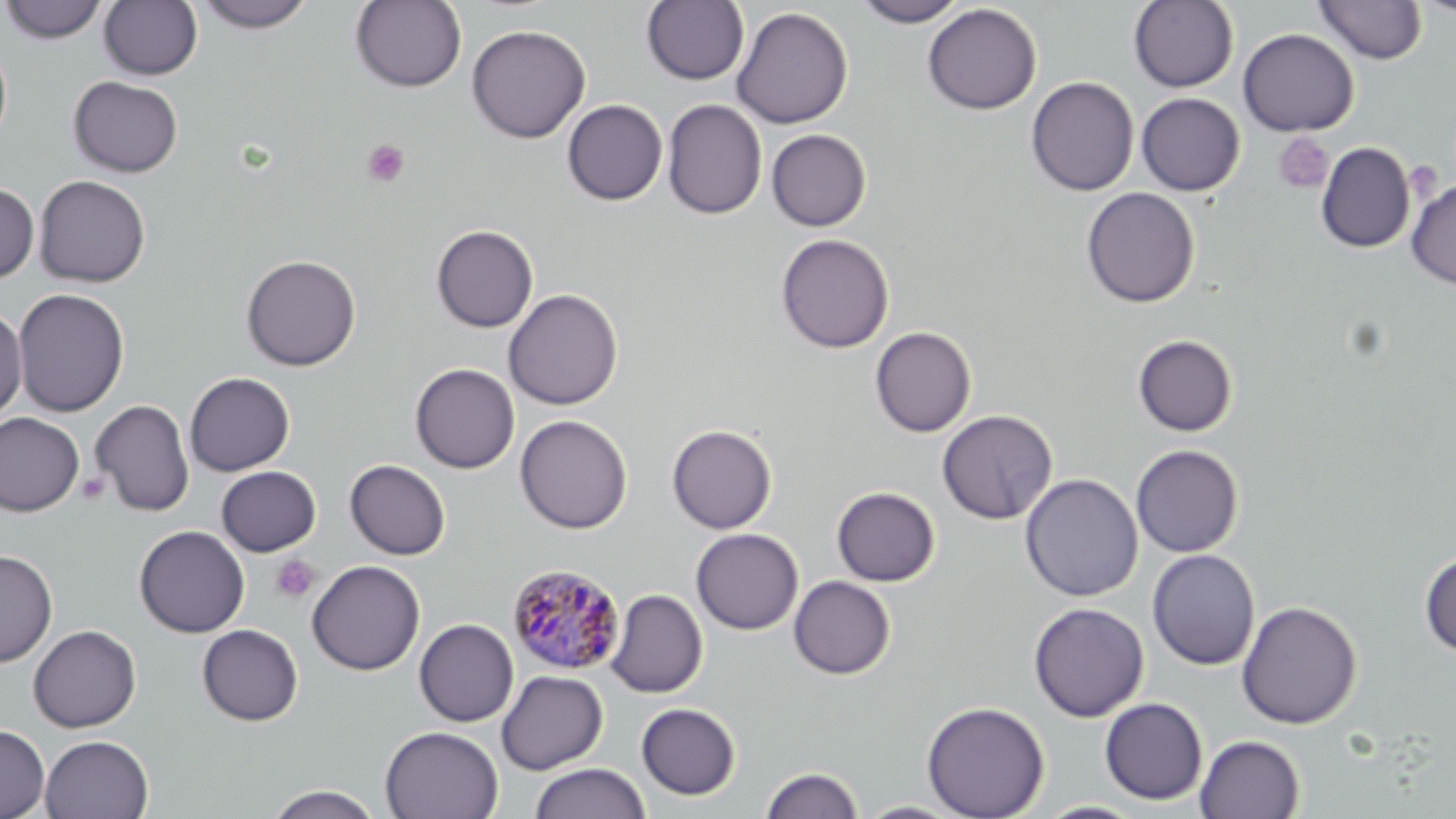

Approximate bounding boxes as named x1/y1/x2/y2 corners in pixels. Uninfected red blood cell locations: (x1=1, y1=0, x2=108, y2=44), (x1=193, y1=0, x2=316, y2=32), (x1=855, y1=0, x2=967, y2=27), (x1=1128, y1=0, x2=1239, y2=93), (x1=1314, y1=0, x2=1427, y2=64), (x1=1412, y1=0, x2=1456, y2=19), (x1=99, y1=1, x2=202, y2=80), (x1=350, y1=1, x2=467, y2=92), (x1=641, y1=1, x2=749, y2=86), (x1=922, y1=4, x2=1042, y2=115), (x1=731, y1=7, x2=854, y2=129), (x1=466, y1=24, x2=591, y2=143), (x1=1237, y1=28, x2=1359, y2=137), (x1=0, y1=40, x2=12, y2=148), (x1=68, y1=76, x2=183, y2=177), (x1=1026, y1=76, x2=1139, y2=196), (x1=1136, y1=92, x2=1245, y2=196), (x1=562, y1=99, x2=668, y2=205), (x1=662, y1=99, x2=767, y2=220), (x1=766, y1=129, x2=871, y2=231), (x1=1316, y1=142, x2=1415, y2=253), (x1=33, y1=175, x2=151, y2=288), (x1=1406, y1=179, x2=1456, y2=289), (x1=0, y1=182, x2=39, y2=284), (x1=1081, y1=187, x2=1200, y2=308), (x1=431, y1=225, x2=538, y2=332), (x1=775, y1=233, x2=894, y2=354), (x1=241, y1=254, x2=361, y2=371), (x1=12, y1=288, x2=129, y2=417), (x1=503, y1=288, x2=623, y2=410), (x1=0, y1=306, x2=28, y2=420), (x1=870, y1=326, x2=976, y2=437), (x1=1133, y1=334, x2=1237, y2=436), (x1=410, y1=363, x2=520, y2=473), (x1=184, y1=372, x2=295, y2=476), (x1=90, y1=399, x2=195, y2=517), (x1=937, y1=410, x2=1057, y2=525), (x1=0, y1=412, x2=85, y2=516), (x1=515, y1=414, x2=632, y2=534), (x1=666, y1=424, x2=777, y2=534), (x1=1131, y1=444, x2=1244, y2=557), (x1=345, y1=459, x2=450, y2=559), (x1=216, y1=466, x2=321, y2=556), (x1=1020, y1=473, x2=1143, y2=602), (x1=831, y1=486, x2=941, y2=586), (x1=134, y1=525, x2=250, y2=638), (x1=690, y1=528, x2=803, y2=635), (x1=1147, y1=548, x2=1260, y2=670), (x1=0, y1=549, x2=58, y2=667), (x1=1419, y1=552, x2=1456, y2=657), (x1=306, y1=559, x2=426, y2=676), (x1=788, y1=576, x2=896, y2=679), (x1=606, y1=588, x2=707, y2=698), (x1=1237, y1=600, x2=1362, y2=729), (x1=1028, y1=602, x2=1149, y2=722), (x1=414, y1=619, x2=519, y2=727), (x1=197, y1=624, x2=304, y2=726), (x1=28, y1=625, x2=141, y2=732), (x1=496, y1=670, x2=608, y2=775), (x1=1099, y1=697, x2=1208, y2=805), (x1=921, y1=700, x2=1049, y2=819), (x1=636, y1=702, x2=741, y2=800), (x1=0, y1=724, x2=50, y2=819), (x1=380, y1=726, x2=504, y2=819), (x1=39, y1=734, x2=153, y2=819), (x1=1195, y1=735, x2=1305, y2=818), (x1=529, y1=763, x2=652, y2=819), (x1=761, y1=766, x2=863, y2=819), (x1=264, y1=784, x2=386, y2=819), (x1=855, y1=801, x2=968, y2=818), (x1=1033, y1=801, x2=1147, y2=818). Platelet locations: (x1=1274, y1=133, x2=1333, y2=194), (x1=362, y1=139, x2=410, y2=187), (x1=271, y1=556, x2=318, y2=603). Plasmodium malariae-infected red blood cell locations: (x1=508, y1=564, x2=625, y2=675). Slide-level diagnosis: Plasmodium malariae. Thin blood smear. One field of a larger specimen. Optical microscopy. Image is 1456×819 pixels. Captured at 1000x magnification. May-Grünwald-Giemsa-stained preparation.